Name the cell type shown.
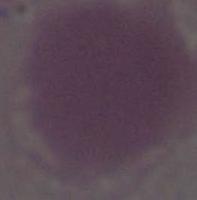
An erythrocyte.

Summary:
  - Modality: micrograph
  - Magnification: 1000x